Classify this cell by malaria status.
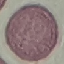

It is uninfected.

stain = Giemsa
image type = cell patch, automatically extracted from a larger field of view and resized to 64 × 64 pixels
preparation = thin smear
capture = smartphone through the microscope eyepiece